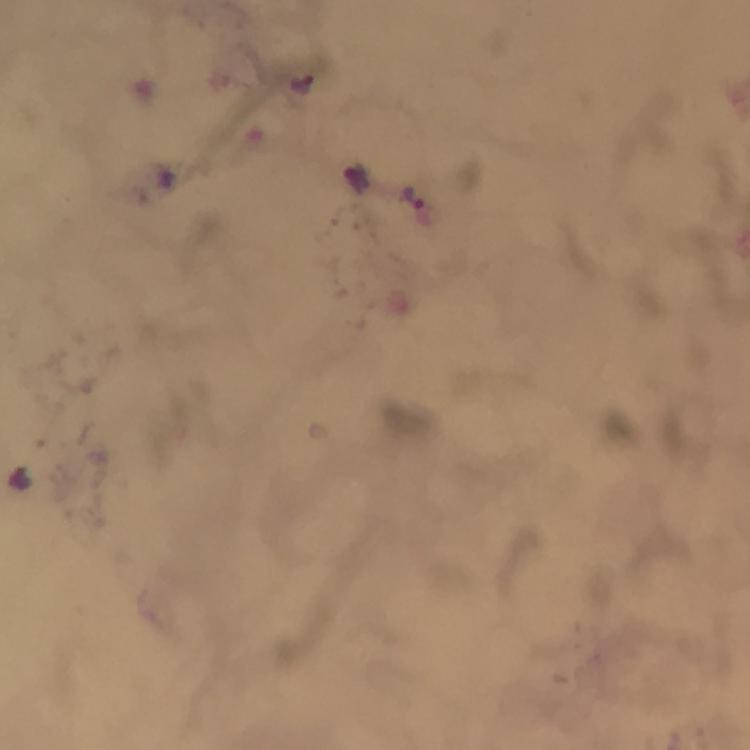
{
  "immersion_oil": "used",
  "cropped_from": "one field of view",
  "plasmodium_parasite_locations": "approximate centers as (x, y) in pixels: (303, 84), (356, 181), (413, 199), (21, 478)",
  "preparation": "thick smear",
  "context": "from a malaria diagnostic workup",
  "stain": "Giemsa",
  "capture": "smartphone camera through the microscope",
  "image_size": "750×750 pixels",
  "magnification": "100x"
}